State which parasite is depicted.
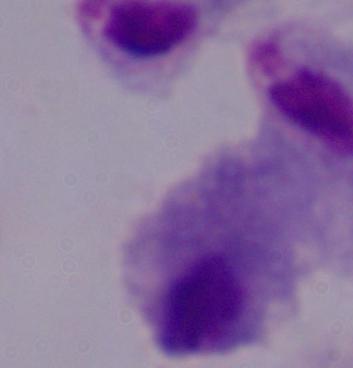
A trichomonad.

Summary:
  - Magnification: 1000x
  - Modality: micrograph